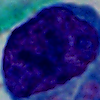

modality = photomicrograph
identification = leukocyte
magnification = 1000x